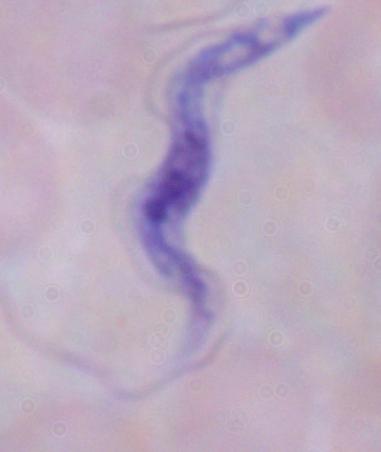
Summary:
  - Modality: photomicrograph
  - Identification: trypanosome
  - Magnification: 1000x